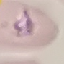

Result: malaria parasites identified. Automatically extracted cell patch, resized to 64 × 64 pixels. Giemsa-stained preparation. Acquired by smartphone through the microscope eyepiece. Thin blood smear.